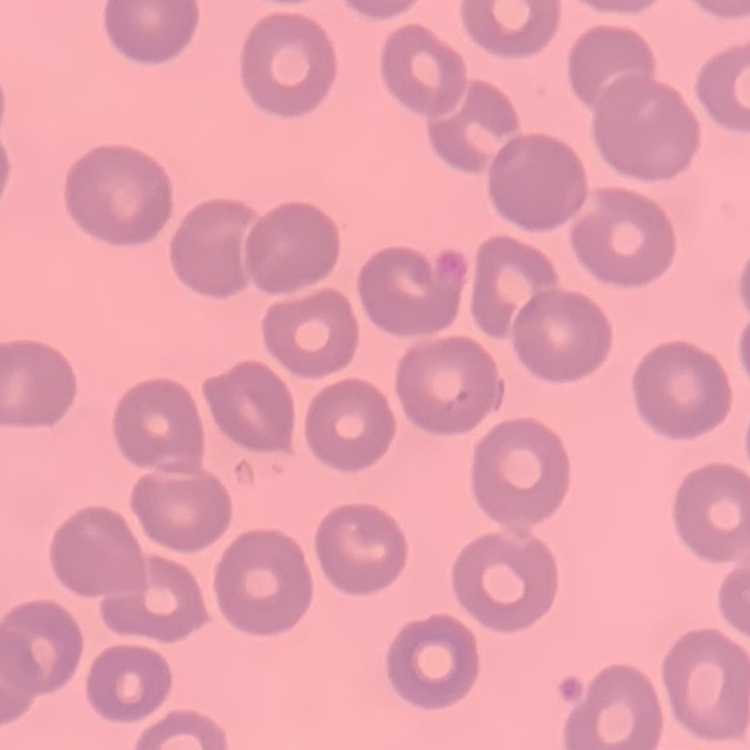 The erythrocytes show no rouleaux formation. One tile cut from a larger photomicrograph. Stained with either Field's or Giemsa. Thin peripheral smear.